State which parasite is depicted.
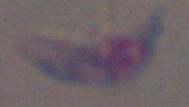
This is Toxoplasma gondii.

Summary:
  - Modality: photomicrograph
  - Magnification: 1000x